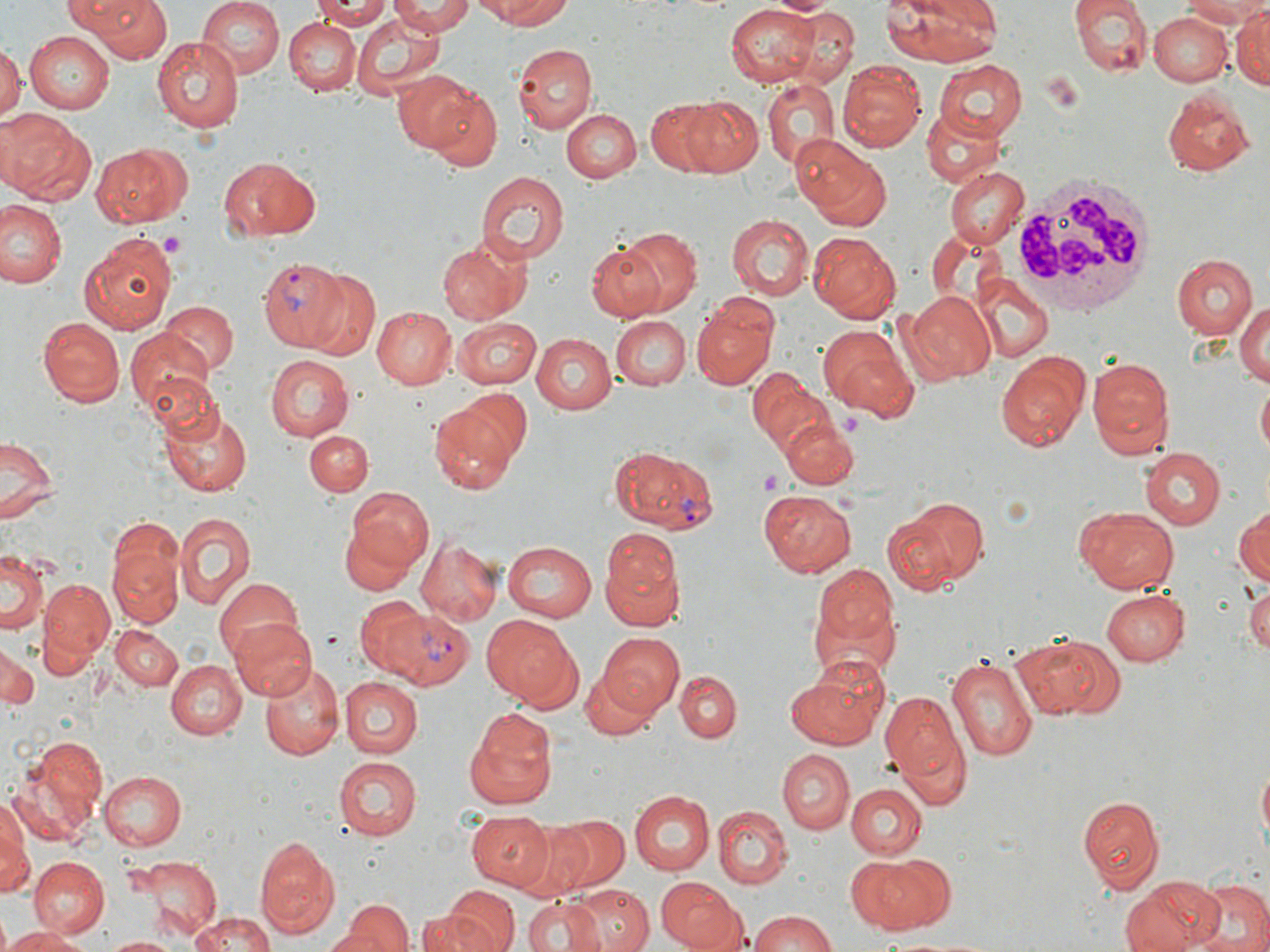

Summary:
  - Coordinate format: approximate bounding boxes as [x1, y1, x2, y2] in pixels
  - Uninfected red blood cell locations: [69, 0, 177, 64], [197, 0, 282, 81], [311, 0, 397, 27], [390, 0, 474, 37], [490, 0, 574, 27], [882, 0, 1006, 66], [1073, 0, 1152, 77], [1178, 0, 1270, 26], [362, 1, 467, 59], [726, 2, 816, 84], [778, 2, 862, 86], [1230, 2, 1270, 88], [353, 12, 446, 95], [1151, 13, 1232, 86], [284, 18, 361, 95], [23, 31, 116, 113], [152, 37, 244, 133], [0, 43, 23, 123], [512, 43, 597, 134], [837, 59, 925, 153], [934, 60, 1026, 140], [394, 72, 483, 154], [759, 80, 841, 168], [429, 88, 503, 168], [1162, 90, 1256, 176], [679, 96, 765, 180], [645, 99, 731, 176], [923, 107, 1003, 187], [562, 108, 641, 183], [1, 110, 96, 206], [794, 140, 894, 230], [92, 142, 191, 226], [220, 156, 317, 242], [945, 169, 1027, 247], [477, 171, 569, 263], [0, 200, 67, 291], [725, 213, 815, 301], [611, 226, 705, 319], [807, 228, 904, 322], [79, 231, 177, 334], [438, 235, 533, 325], [585, 240, 673, 323], [1171, 253, 1257, 340], [300, 270, 383, 362], [973, 277, 1052, 362], [901, 288, 997, 383], [692, 297, 779, 389], [1236, 298, 1270, 390], [161, 301, 237, 376], [373, 306, 455, 389], [613, 316, 690, 390], [39, 317, 125, 407], [454, 318, 541, 389], [545, 321, 692, 400], [819, 325, 916, 417], [125, 330, 215, 418], [533, 331, 619, 413], [993, 350, 1090, 452], [265, 353, 354, 439], [1086, 356, 1173, 457], [745, 367, 825, 454], [1255, 382, 1269, 460], [450, 389, 529, 464], [160, 400, 255, 497], [429, 405, 519, 494], [777, 415, 859, 489], [305, 430, 373, 496], [0, 433, 61, 526], [1138, 446, 1226, 529], [761, 487, 855, 576], [347, 489, 433, 571], [889, 495, 992, 591], [1073, 506, 1179, 594], [1233, 508, 1269, 587], [173, 514, 254, 610], [338, 522, 419, 595], [600, 531, 681, 625], [415, 535, 504, 626], [501, 541, 595, 620], [108, 542, 182, 627], [1, 550, 49, 634], [809, 566, 902, 682], [214, 575, 304, 662], [37, 577, 113, 669], [1245, 584, 1270, 654], [1100, 588, 1191, 667], [355, 598, 434, 680], [482, 614, 579, 706], [230, 618, 317, 702], [112, 626, 185, 689], [596, 632, 686, 716], [1015, 633, 1120, 722], [0, 646, 37, 713], [945, 652, 1038, 765], [785, 658, 891, 751], [167, 660, 245, 739], [261, 660, 343, 761], [580, 665, 662, 739], [675, 671, 741, 740], [783, 677, 871, 833], [341, 678, 423, 758], [881, 686, 969, 800], [468, 710, 558, 805], [12, 735, 111, 843], [776, 747, 855, 832], [333, 756, 423, 838], [1254, 758, 1269, 853], [99, 772, 188, 851], [846, 782, 926, 859], [629, 790, 714, 874], [1077, 792, 1165, 893], [0, 797, 36, 898], [715, 807, 793, 887], [469, 812, 554, 888], [553, 815, 630, 892], [508, 819, 595, 902], [255, 836, 339, 939], [846, 853, 955, 935], [131, 855, 220, 940], [28, 857, 109, 938], [1120, 875, 1224, 952], [1188, 877, 1270, 952], [658, 879, 745, 952], [569, 885, 655, 952], [424, 896, 518, 952], [523, 897, 603, 952], [336, 899, 414, 952], [748, 910, 839, 951], [185, 913, 281, 952], [417, 913, 479, 950], [3, 927, 89, 952], [105, 935, 181, 952]
  - Platelet locations: [159, 229, 184, 258], [759, 470, 784, 491]
  - White blood cell locations: [1009, 173, 1153, 316]
  - Plasmodium vivax-infected red blood cell locations: [258, 258, 356, 352], [611, 445, 718, 534], [377, 607, 475, 690]
  - Slide-level diagnosis: Plasmodium vivax
  - Magnification: 1000x
  - Stain: May-Grünwald-Giemsa
  - Image size: 1270×952 pixels
  - Preparation: thin blood film
  - Modality: light microscopy
  - Field of view: single